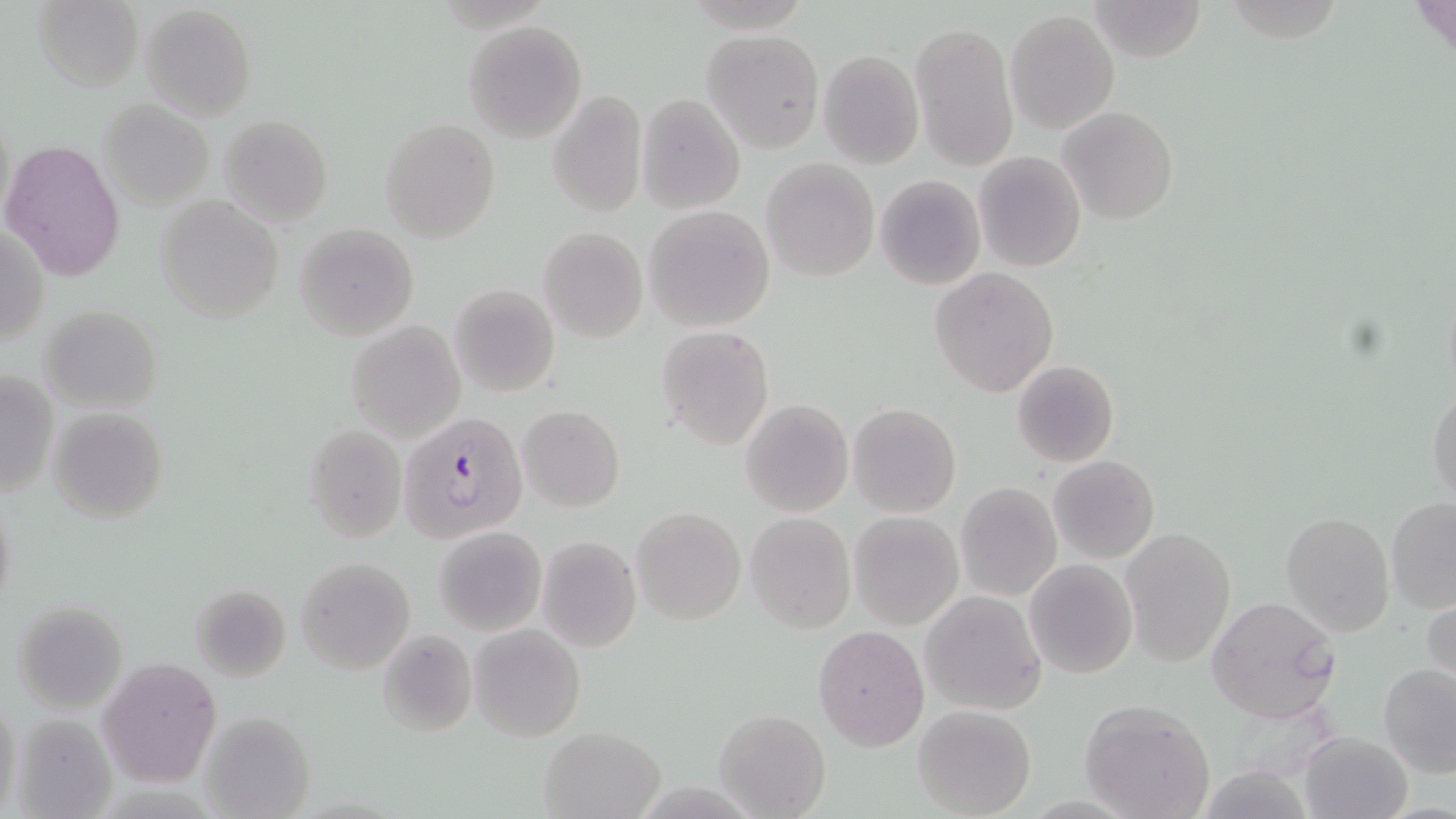
Summary:
  - Coordinate format: approximate bounding boxes as named x1/y1/x2/y2 corners in pixels
  - Uninfected red blood cell locations: (x1=32, y1=0, x2=143, y2=90), (x1=1086, y1=0, x2=1206, y2=62), (x1=1411, y1=0, x2=1453, y2=55), (x1=141, y1=4, x2=256, y2=119), (x1=1006, y1=8, x2=1119, y2=134), (x1=910, y1=19, x2=1018, y2=172), (x1=464, y1=20, x2=587, y2=142), (x1=702, y1=31, x2=824, y2=152), (x1=818, y1=49, x2=924, y2=170), (x1=800, y1=63, x2=912, y2=249), (x1=547, y1=89, x2=646, y2=217), (x1=636, y1=91, x2=746, y2=214), (x1=98, y1=100, x2=213, y2=208), (x1=1059, y1=106, x2=1178, y2=225), (x1=219, y1=114, x2=333, y2=227), (x1=381, y1=117, x2=499, y2=243), (x1=1, y1=139, x2=125, y2=282), (x1=973, y1=151, x2=1086, y2=273), (x1=761, y1=157, x2=880, y2=281), (x1=874, y1=174, x2=987, y2=290), (x1=156, y1=195, x2=285, y2=324), (x1=643, y1=205, x2=774, y2=331), (x1=293, y1=223, x2=419, y2=341), (x1=537, y1=226, x2=648, y2=344), (x1=2, y1=227, x2=48, y2=347), (x1=929, y1=268, x2=1058, y2=397), (x1=448, y1=284, x2=560, y2=396), (x1=38, y1=304, x2=160, y2=413), (x1=345, y1=320, x2=467, y2=442), (x1=656, y1=326, x2=774, y2=448), (x1=1012, y1=360, x2=1120, y2=468), (x1=0, y1=369, x2=57, y2=498), (x1=1428, y1=386, x2=1456, y2=512), (x1=740, y1=399, x2=853, y2=516), (x1=849, y1=402, x2=961, y2=516), (x1=518, y1=404, x2=625, y2=511), (x1=47, y1=406, x2=169, y2=524), (x1=303, y1=423, x2=408, y2=544), (x1=1049, y1=455, x2=1159, y2=562), (x1=955, y1=481, x2=1061, y2=601), (x1=1, y1=489, x2=17, y2=618), (x1=1386, y1=496, x2=1456, y2=611), (x1=632, y1=507, x2=745, y2=625), (x1=1281, y1=510, x2=1394, y2=637), (x1=744, y1=511, x2=856, y2=634), (x1=849, y1=511, x2=963, y2=629), (x1=434, y1=525, x2=547, y2=636), (x1=1121, y1=528, x2=1235, y2=666), (x1=536, y1=535, x2=641, y2=652), (x1=295, y1=557, x2=414, y2=673), (x1=1024, y1=559, x2=1138, y2=678), (x1=192, y1=584, x2=293, y2=682), (x1=1424, y1=588, x2=1455, y2=701), (x1=922, y1=590, x2=1047, y2=716), (x1=1206, y1=596, x2=1345, y2=726), (x1=10, y1=599, x2=129, y2=713), (x1=469, y1=624, x2=586, y2=742), (x1=813, y1=624, x2=929, y2=752), (x1=375, y1=630, x2=476, y2=735), (x1=97, y1=658, x2=221, y2=788), (x1=1378, y1=662, x2=1456, y2=778), (x1=1, y1=693, x2=21, y2=819), (x1=1080, y1=700, x2=1217, y2=819), (x1=913, y1=705, x2=1037, y2=818), (x1=197, y1=708, x2=319, y2=819), (x1=715, y1=708, x2=831, y2=818), (x1=7, y1=712, x2=117, y2=818), (x1=539, y1=726, x2=664, y2=818), (x1=1299, y1=731, x2=1415, y2=819)
  - Plasmodium falciparum-infected red blood cell locations: (x1=399, y1=409, x2=527, y2=543)
  - Slide-level diagnosis: Plasmodium falciparum
  - Field of view: single
  - Image size: 1456×819 pixels
  - Magnification: 1000x
  - Stain: May-Grünwald-Giemsa
  - Preparation: thin blood film
  - Modality: light microscopy